Report the malaria status of this cell.
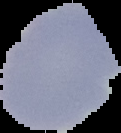
Uninfected.

Summary:
  - Image size: 121×133 pixels
  - Preparation: thin blood film
  - Image type: segmented cell region with the area outside set to black